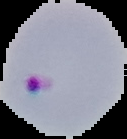

Segmented cell region on a black background. Image is 127×139 pixels. Malaria status: parasitized. From a thin blood smear.